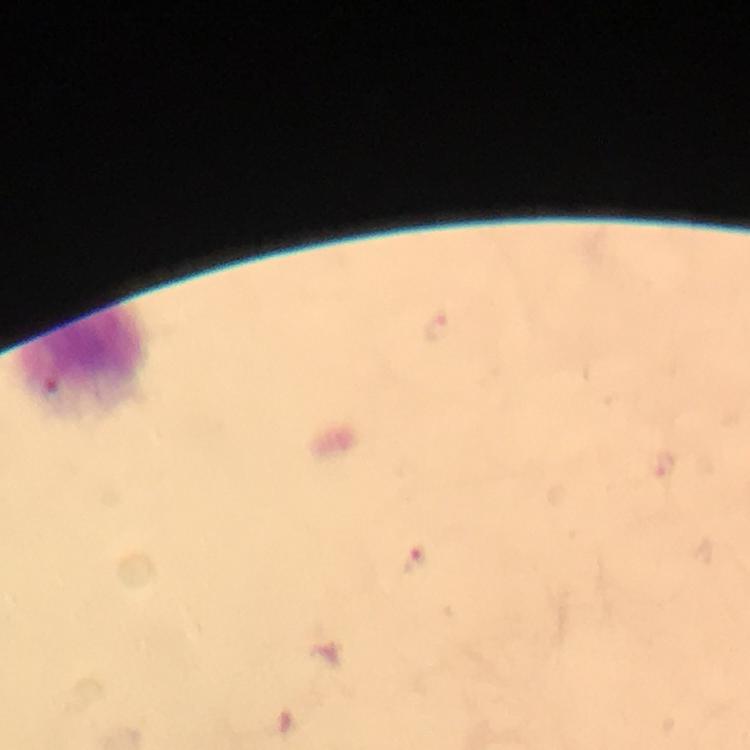

Approximate centers as {x, y} in pixels. Leukocyte locations: {86, 358}. Malaria parasite locations: {417, 562}. Giemsa-stained preparation. 100x magnification. From a malaria diagnostic workup. A crop from one field of view. Thick blood film. Photographed with a smartphone mounted on the microscope. Image is 750×750 pixels. Immersion oil was used.